Rate the background quality.
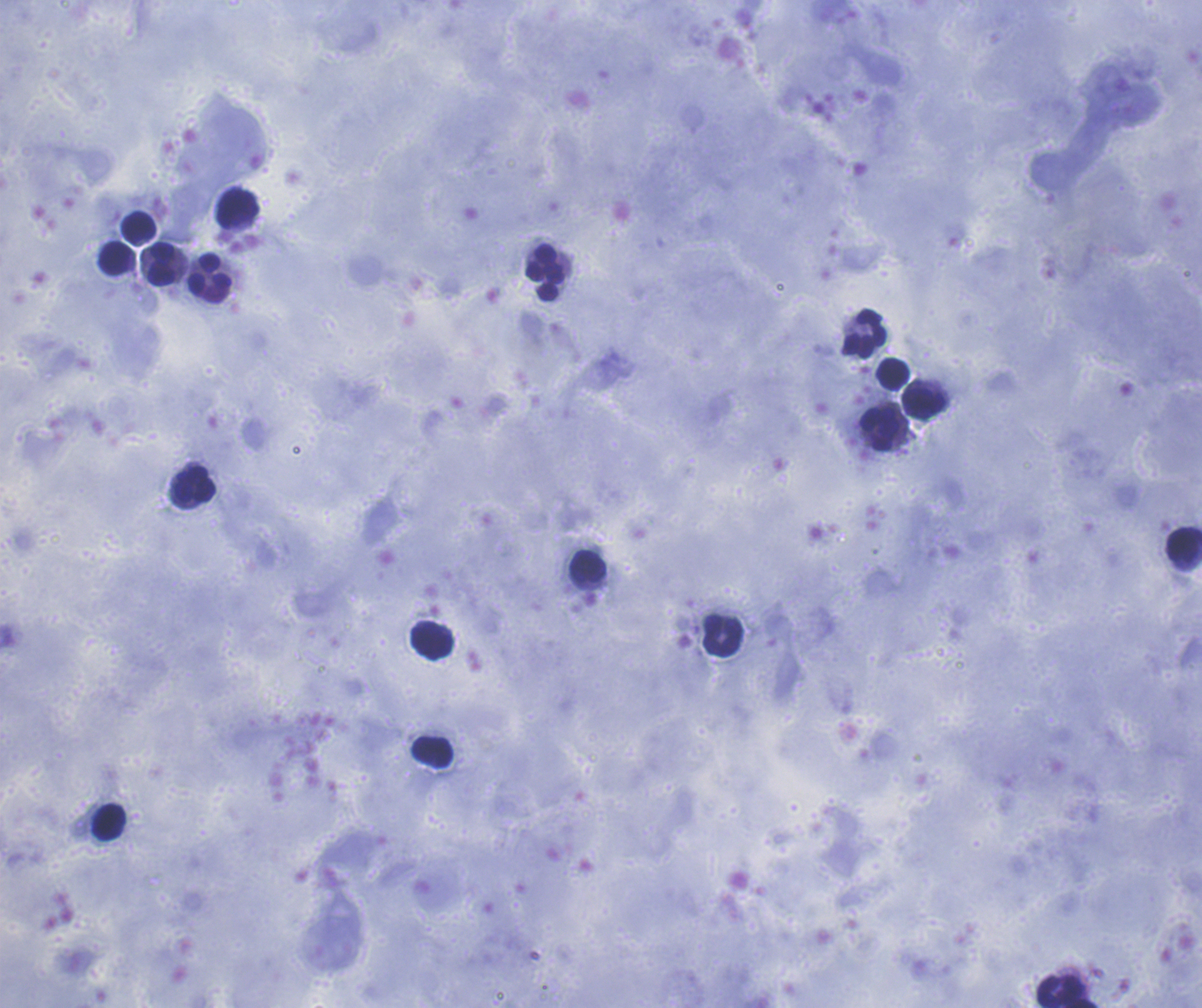
It is good.

Approximate object centers, in pixels from the top-left corner.
Summary:
  - Leukocyte locations: (x=238, y=208), (x=139, y=227), (x=116, y=258), (x=163, y=263), (x=545, y=272), (x=210, y=273), (x=863, y=334), (x=891, y=374), (x=924, y=401), (x=881, y=430), (x=194, y=484), (x=1182, y=545), (x=588, y=566), (x=722, y=635), (x=431, y=642), (x=432, y=751), (x=109, y=822), (x=1061, y=990)
  - Coloration quality: good
  - Stain: Romanowsky
  - Field of view: one from this slide
  - Image size: 1202×1008 pixels
  - Context: previously used in a real diagnosis
  - Preparation: thick blood smear
  - Result: no Plasmodium parasites detected
  - Magnification: 100x